Classify this cell by malaria status.
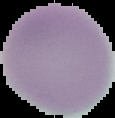

It is uninfected.

Summary:
  - Image size: 115×118 pixels
  - Image type: cell region segmented out of the field of view; surrounding area masked to black
  - Preparation: thin blood film